Comment on the morphology of the erythrocytes.
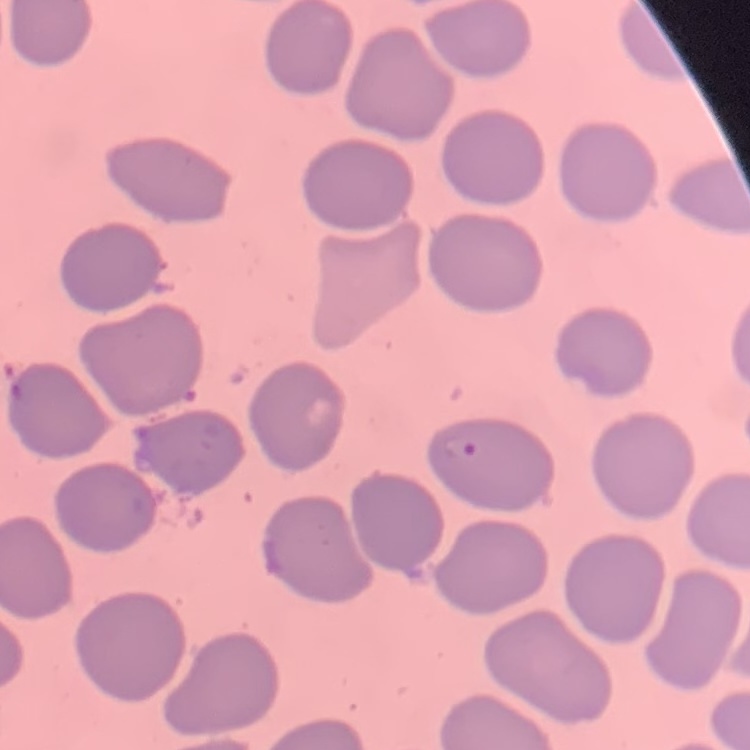
They show no rouleaux formation.

image type = square crop of a larger photomicrograph
stain = Field's or Giemsa
preparation = thin blood smear